Assess this cell for malaria.
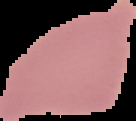

Uninfected.

preparation: thin blood film
image_size: 136×121 pixels
image_type: segmented cell region with the area outside set to black